Name the parasite shown.
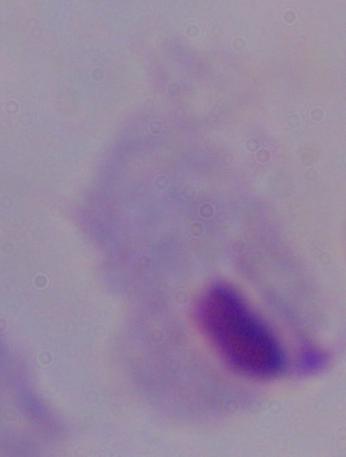
A trichomonad.

magnification = 1000x
modality = photomicrograph